Name the parasite shown.
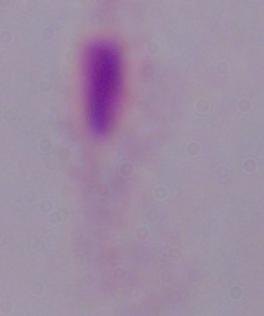

A trichomonad.

magnification = 1000x
modality = micrograph